Assess this cell for malaria.
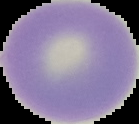
It is uninfected.

Image is 139×124 pixels. The area outside the segmented cell region is set to black. From a thin blood smear.